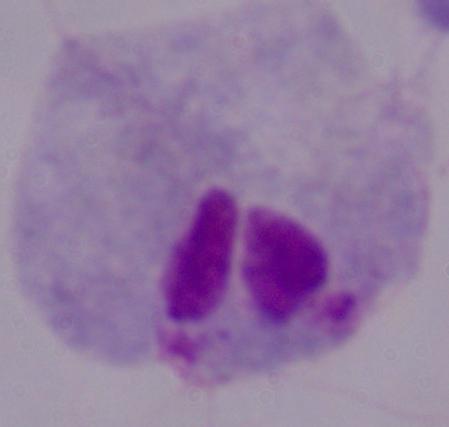
Summary:
  - Modality: photomicrograph
  - Magnification: 1000x
  - Identification: trichomonad